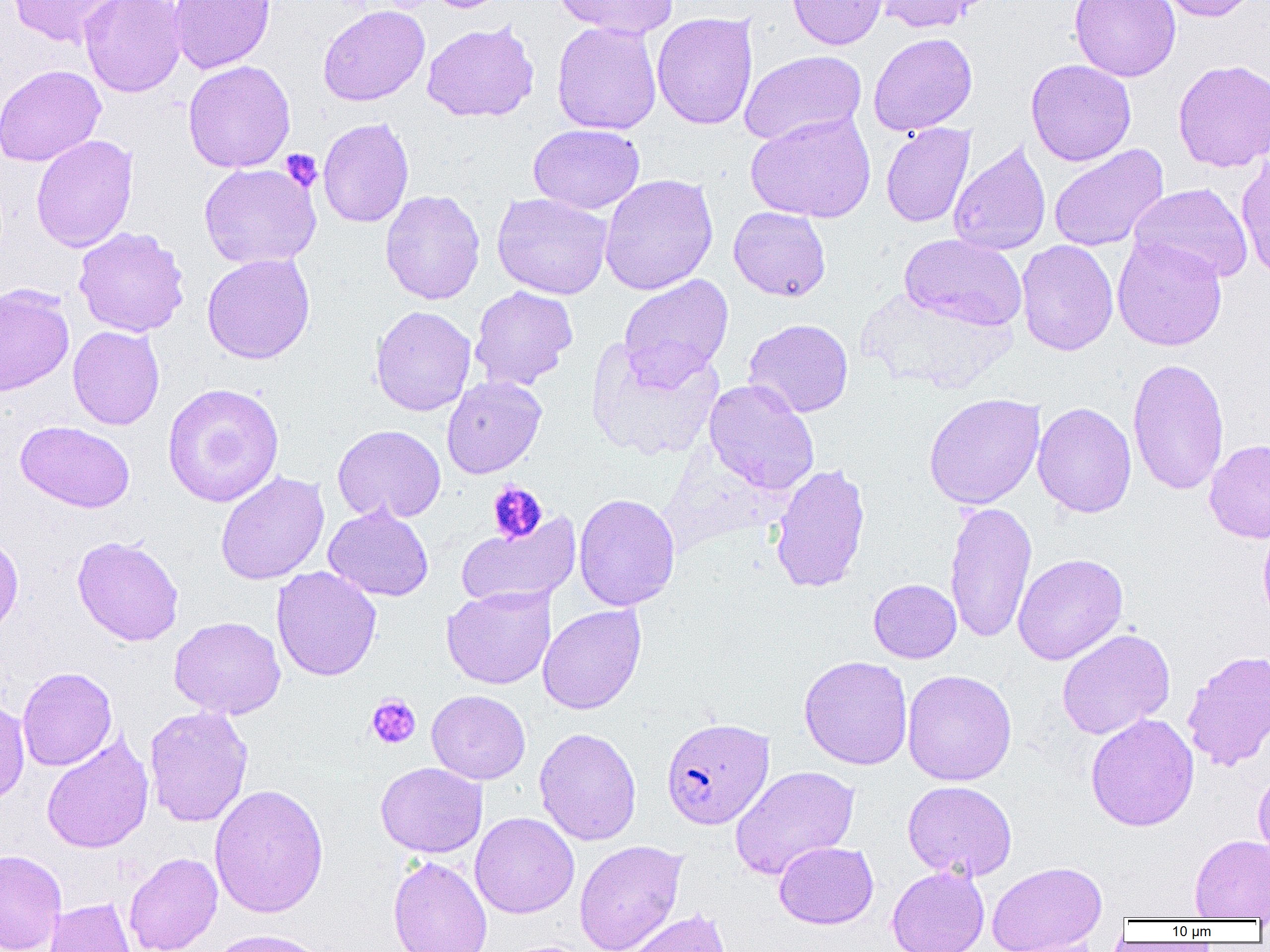
Summary:
  - Coordinate format: approximate bounding boxes as named x1/y1/x2/y2 corners in pixels
  - Platelet locations: (x1=281, y1=149, x2=323, y2=192), (x1=487, y1=481, x2=548, y2=544), (x1=366, y1=694, x2=421, y2=749)
  - Plasmodium falciparum-infected red blood cell locations: (x1=661, y1=716, x2=774, y2=830)
  - Uninfected red blood cell locations: (x1=7, y1=0, x2=126, y2=48), (x1=78, y1=0, x2=187, y2=97), (x1=168, y1=0, x2=275, y2=74), (x1=427, y1=0, x2=512, y2=13), (x1=553, y1=0, x2=679, y2=38), (x1=787, y1=0, x2=889, y2=50), (x1=873, y1=0, x2=989, y2=34), (x1=1069, y1=0, x2=1181, y2=82), (x1=1153, y1=0, x2=1259, y2=22), (x1=318, y1=5, x2=430, y2=107), (x1=652, y1=12, x2=758, y2=130), (x1=421, y1=21, x2=539, y2=123), (x1=552, y1=21, x2=662, y2=135), (x1=868, y1=32, x2=977, y2=136), (x1=739, y1=50, x2=867, y2=146), (x1=1026, y1=59, x2=1136, y2=166), (x1=1173, y1=59, x2=1270, y2=172), (x1=183, y1=60, x2=296, y2=173), (x1=0, y1=65, x2=106, y2=166), (x1=745, y1=112, x2=876, y2=223), (x1=318, y1=118, x2=414, y2=228), (x1=528, y1=123, x2=645, y2=215), (x1=881, y1=123, x2=975, y2=228), (x1=30, y1=134, x2=139, y2=253), (x1=948, y1=140, x2=1051, y2=256), (x1=1048, y1=145, x2=1169, y2=252), (x1=1236, y1=152, x2=1270, y2=282), (x1=198, y1=163, x2=322, y2=269), (x1=599, y1=173, x2=718, y2=295), (x1=1129, y1=183, x2=1253, y2=284), (x1=380, y1=190, x2=485, y2=305), (x1=492, y1=193, x2=613, y2=300), (x1=728, y1=206, x2=831, y2=301), (x1=73, y1=227, x2=190, y2=337), (x1=899, y1=233, x2=1027, y2=331), (x1=1112, y1=236, x2=1228, y2=351), (x1=1016, y1=240, x2=1118, y2=356), (x1=201, y1=253, x2=316, y2=364), (x1=618, y1=274, x2=734, y2=388), (x1=0, y1=284, x2=75, y2=396), (x1=470, y1=285, x2=578, y2=391), (x1=853, y1=289, x2=1016, y2=394), (x1=370, y1=305, x2=476, y2=416), (x1=743, y1=318, x2=854, y2=417), (x1=67, y1=325, x2=165, y2=430), (x1=587, y1=337, x2=724, y2=461), (x1=1127, y1=359, x2=1229, y2=495), (x1=442, y1=375, x2=547, y2=479), (x1=703, y1=379, x2=820, y2=495), (x1=162, y1=383, x2=284, y2=508), (x1=923, y1=393, x2=1045, y2=509), (x1=1032, y1=402, x2=1137, y2=518), (x1=15, y1=420, x2=135, y2=513), (x1=332, y1=424, x2=446, y2=524), (x1=1204, y1=439, x2=1270, y2=543), (x1=769, y1=462, x2=871, y2=594), (x1=215, y1=471, x2=330, y2=585), (x1=573, y1=493, x2=680, y2=611), (x1=945, y1=500, x2=1037, y2=644), (x1=323, y1=505, x2=434, y2=602), (x1=455, y1=514, x2=581, y2=609), (x1=1257, y1=519, x2=1270, y2=628), (x1=0, y1=533, x2=24, y2=641), (x1=72, y1=535, x2=184, y2=646), (x1=1012, y1=553, x2=1128, y2=665), (x1=271, y1=566, x2=382, y2=681), (x1=868, y1=579, x2=961, y2=663), (x1=442, y1=585, x2=555, y2=689), (x1=537, y1=604, x2=647, y2=715), (x1=168, y1=616, x2=286, y2=719), (x1=1056, y1=628, x2=1175, y2=740), (x1=1182, y1=650, x2=1270, y2=771), (x1=798, y1=655, x2=913, y2=770), (x1=17, y1=667, x2=117, y2=771), (x1=902, y1=669, x2=1016, y2=786), (x1=426, y1=690, x2=531, y2=784), (x1=0, y1=695, x2=29, y2=806), (x1=144, y1=705, x2=253, y2=827), (x1=1085, y1=713, x2=1199, y2=832), (x1=534, y1=727, x2=642, y2=846), (x1=41, y1=733, x2=154, y2=854), (x1=375, y1=762, x2=488, y2=858), (x1=729, y1=765, x2=860, y2=881), (x1=1253, y1=767, x2=1270, y2=866), (x1=902, y1=780, x2=1018, y2=881), (x1=208, y1=783, x2=329, y2=919), (x1=470, y1=812, x2=580, y2=919), (x1=1189, y1=834, x2=1270, y2=920), (x1=574, y1=839, x2=687, y2=952), (x1=774, y1=841, x2=878, y2=929), (x1=0, y1=849, x2=67, y2=952), (x1=123, y1=852, x2=223, y2=952), (x1=388, y1=855, x2=492, y2=952), (x1=986, y1=861, x2=1107, y2=951), (x1=887, y1=865, x2=990, y2=952), (x1=45, y1=897, x2=136, y2=952), (x1=620, y1=908, x2=733, y2=952), (x1=208, y1=928, x2=331, y2=952), (x1=1003, y1=936, x2=1105, y2=952), (x1=499, y1=939, x2=600, y2=952)
  - Slide-level diagnosis: Plasmodium falciparum
  - Preparation: thin blood smear
  - Image size: 1270×952 pixels
  - Modality: light microscopy
  - Magnification: 1000x
  - Field of view: single